Classify this cell by malaria status.
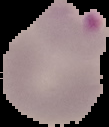

Parasitized.

Summary:
  - Image type: segmented cell region with the area outside set to black
  - Image size: 109×127 pixels
  - Preparation: thin blood film